State which parasite is depicted.
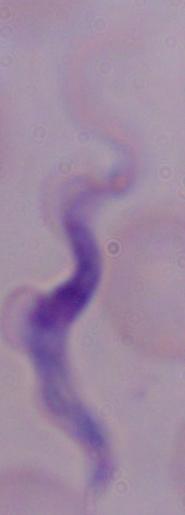
A trypanosome.

Photomicrograph. 1000x magnification.